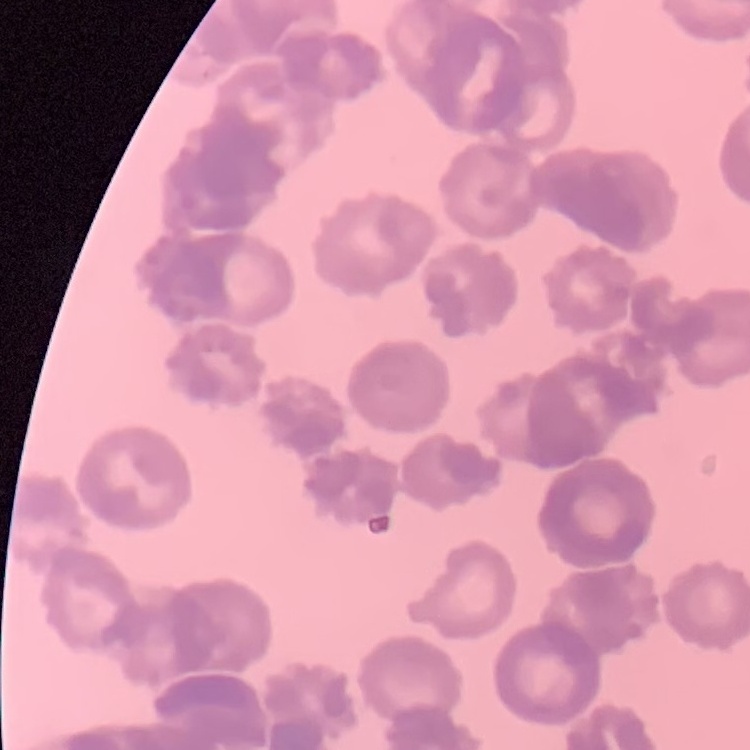
The red blood cells exhibit rouleaux formation. Thin blood film. One tile cut from a larger photomicrograph. Stained with either Field's or Giemsa.